Assess this cell for malaria.
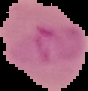
It is parasitized.

Summary:
  - Image size: 88×91 pixels
  - Image type: cell region segmented out of the field of view; surrounding area masked to black
  - Preparation: thin blood smear